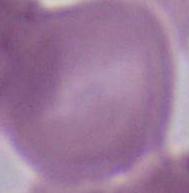
identification = red blood cell
magnification = 1000x
modality = micrograph